Name the parasite shown.
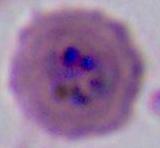

Plasmodium.

magnification: 400x or 1000x
modality: photomicrograph